Describe the morphology of the red blood cells.
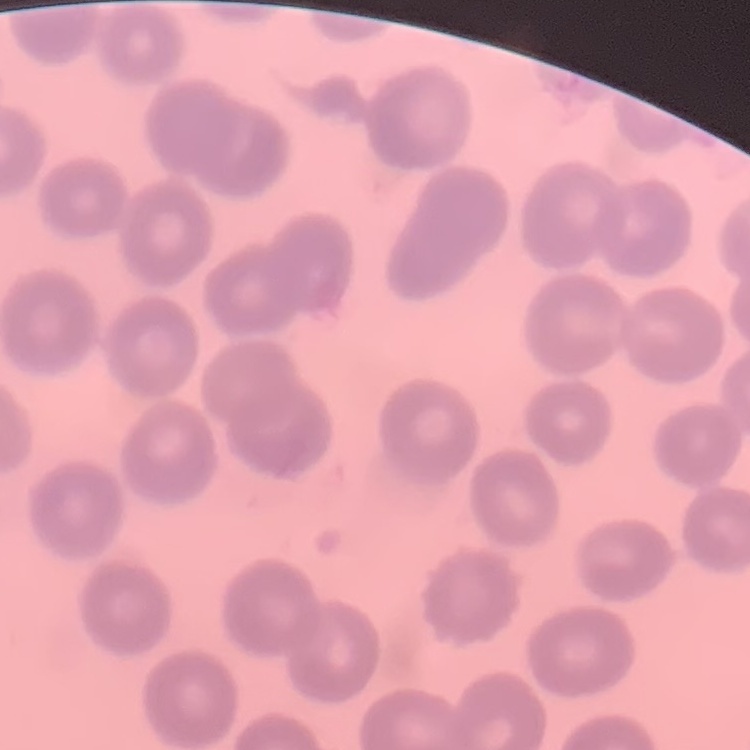

No rouleaux formation.

Field's or Giemsa stain. Thin blood smear. One tile cut from a larger photomicrograph.